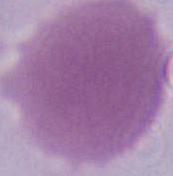
Micrograph. An erythrocyte is seen. 1000x magnification.